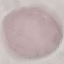

Summary:
  - Result: negative for malaria parasites
  - Image type: cell patch, automatically extracted from a larger field of view and resized to 64 × 64 pixels
  - Capture: smartphone camera at the microscope eyepiece
  - Stain: Giemsa
  - Preparation: thin smear